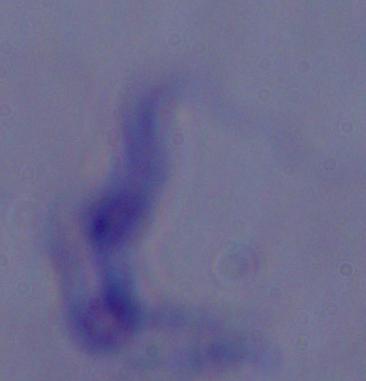
modality = photomicrograph
magnification = 1000x
identification = trypanosome